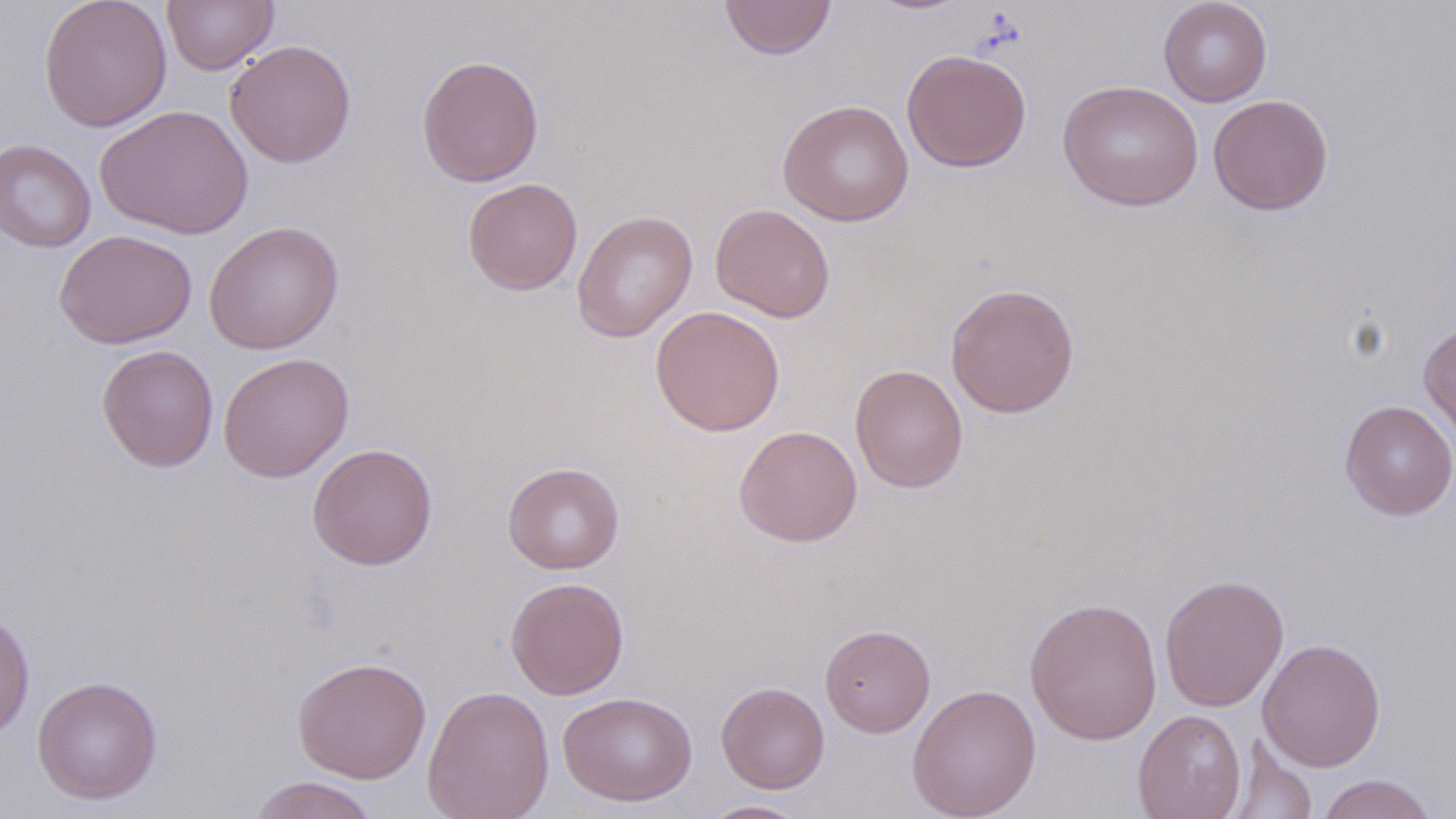

Approximate bounding boxes as (x1,y1)-(x2,y2) corner pairs in pixels. Uninfected red blood cell locations: (38,0)-(173,132), (161,0)-(279,74), (719,0)-(837,60), (1158,0)-(1272,107), (225,39)-(357,167), (901,49)-(1032,173), (417,54)-(544,187), (1058,80)-(1204,211), (1207,94)-(1334,216), (777,100)-(914,226), (95,104)-(254,239), (0,138)-(97,253), (462,177)-(583,296), (710,203)-(836,323), (571,209)-(698,342), (204,220)-(345,355), (54,229)-(197,349), (945,282)-(1080,418), (650,305)-(785,436), (1418,320)-(1456,448), (96,344)-(219,473), (218,352)-(354,482), (850,364)-(968,493), (1339,399)-(1456,521), (733,425)-(863,547), (307,443)-(438,570), (503,461)-(624,574), (1159,573)-(1289,712), (505,576)-(630,700), (1024,596)-(1163,745), (0,607)-(35,744), (820,624)-(935,737), (1258,638)-(1386,771), (292,656)-(432,783), (32,676)-(163,804), (716,681)-(829,793), (906,683)-(1041,819), (422,685)-(555,819), (558,690)-(698,806), (1133,709)-(1247,819), (1229,740)-(1318,818), (1314,773)-(1439,819), (247,776)-(381,819), (697,799)-(813,818). Slide-level diagnosis: negative for blood parasites. May-Grünwald-Giemsa stain. 1000x magnification. One field of a larger specimen. Thin blood film. Optical microscopy. Image is 1456×819 pixels.